Locate every malaria parasite and every leukocyte.
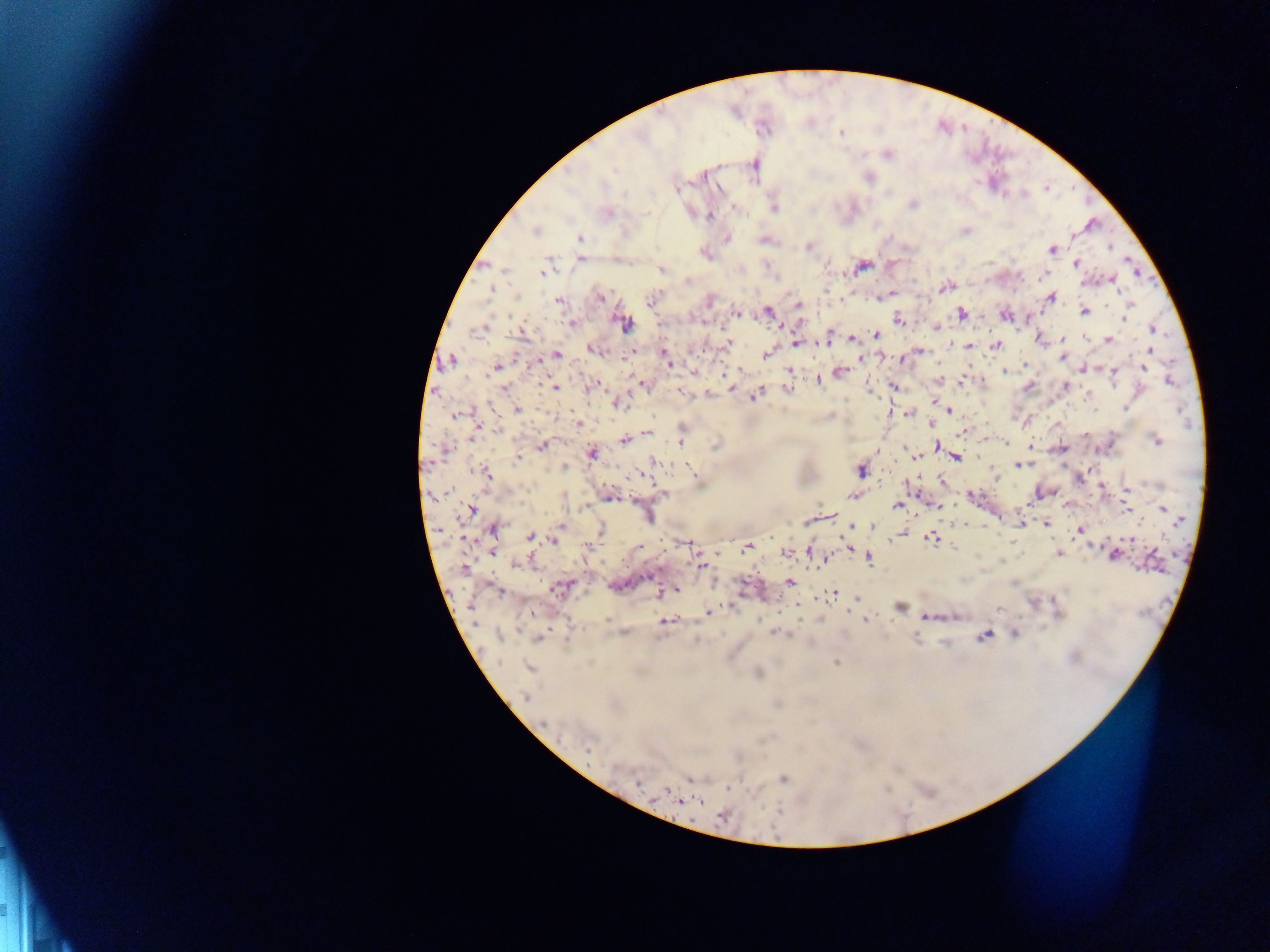

Approximate centers as {x, y} in pixels.
Malaria parasites: {841, 133}, {887, 154}, {704, 176}, {869, 177}, {677, 189}, {624, 193}, {912, 206}, {774, 207}, {734, 208}, {608, 214}, {709, 216}, {1090, 224}, {535, 231}, {966, 231}, {580, 238}, {727, 238}, {809, 247}, {1110, 247}, {1053, 249}, {706, 254}, {581, 259}, {1076, 264}, {861, 267}, {502, 269}, {545, 270}, {662, 270}, {1041, 277}, {1112, 280}, {945, 286}, {491, 290}, {600, 297}, {1050, 298}, {710, 300}, {558, 301}, {652, 301}, {798, 305}, {1129, 305}, {1084, 311}, {768, 312}, {737, 313}, {961, 313}, {1005, 316}, {1124, 317}, {899, 320}, {624, 323}, {571, 324}, {937, 327}, {482, 328}, {1152, 328}, {521, 334}, {876, 334}, {853, 338}, {1039, 338}, {1063, 339}, {1109, 339}, {827, 340}, {796, 343}, {728, 344}, {969, 345}, {997, 345}, {591, 350}, {920, 351}, {632, 352}, {664, 353}, {557, 355}, {766, 355}, {861, 358}, {1062, 358}, {666, 359}, {452, 360}, {539, 361}, {669, 364}, {1025, 364}, {496, 367}, {1144, 368}, {1084, 369}, {789, 370}, {1004, 371}, {839, 372}, {1113, 373}, {725, 375}, {819, 380}, {939, 380}, {1169, 381}, {961, 382}, {596, 384}, {642, 384}, {893, 386}, {1029, 386}, {1066, 386}, {555, 388}, {731, 388}, {788, 388}, {505, 389}, {679, 392}, {756, 395}, {934, 401}, {617, 403}, {1125, 408}, {949, 409}, {517, 410}, {908, 414}, {457, 415}, {578, 424}, {478, 426}, {933, 426}, {499, 430}, {964, 432}, {647, 434}, {1085, 435}, {472, 438}, {1156, 440}, {624, 441}, {681, 442}, {1006, 443}, {542, 445}, {938, 446}, {592, 452}, {916, 455}, {956, 458}, {518, 460}, {653, 460}, {1020, 465}, {565, 467}, {691, 470}, {861, 470}, {487, 475}, {942, 481}, {1101, 486}, {1127, 489}, {663, 493}, {853, 496}, {609, 497}, {897, 505}, {936, 506}, {1125, 506}, {1163, 509}, {471, 510}, {1020, 523}, {1046, 524}, {561, 526}, {871, 526}, {494, 529}, {601, 530}, {1079, 532}, {530, 536}, {901, 536}, {931, 538}, {1131, 538}, {554, 540}, {688, 545}, {847, 546}, {639, 547}, {747, 547}, {589, 548}, {810, 552}, {786, 554}, {1059, 554}, {1113, 555}, {870, 558}, {827, 559}, {701, 564}, {514, 565}, {464, 569}, {649, 577}, {790, 581}, {560, 588}, {498, 591}, {676, 591}, {659, 593}, {834, 594}, {731, 607}, {900, 607}, {532, 612}, {708, 612}, {927, 617}, {607, 619}, {821, 619}, {865, 620}, {666, 621}, {1015, 633}, {775, 634}, {984, 636}, {538, 638}, {836, 663}, {528, 667}, {757, 672}, {525, 697}, {543, 723}, {588, 750}, {784, 778}, {691, 779}, {638, 784}, {682, 801}, {722, 816}.
No leukocytes observed.

Summary:
  - Preparation: thick blood smear
  - Image size: 1270×952 pixels
  - Capture: mobile-phone photograph through a microscope
  - Field of view: single
  - Country: Ghana